Outline each blood parasite and name the species.
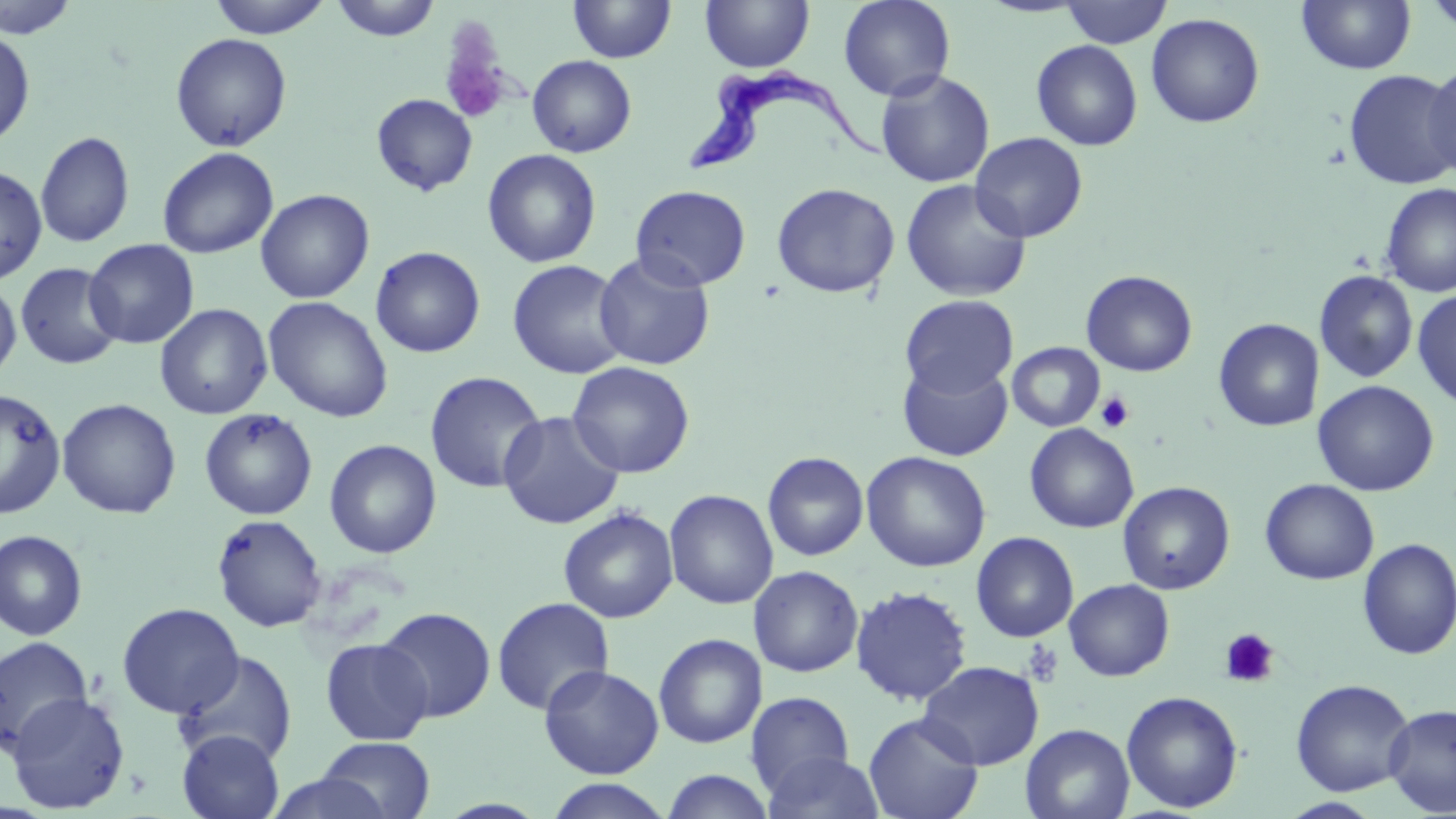

Approximate bounding boxes as (x1,y1)-(x2,y2) corner pairs in pixels.
Trypanosoma brucei: (683,72)-(892,177).
No Plasmodium falciparum, Plasmodium ovale, Plasmodium malariae, Plasmodium vivax, or Babesia divergens observed.

Platelet locations: (438,26)-(513,125), (1095,391)-(1134,433), (1219,628)-(1279,687), (1022,640)-(1064,688). Uninfected red blood cell locations: (0,0)-(82,39), (206,0)-(333,38), (329,0)-(442,41), (568,0)-(676,63), (699,0)-(815,73), (838,0)-(956,101), (1059,0)-(1172,48), (1297,0)-(1416,75), (1421,0)-(1456,37), (1146,13)-(1265,128), (0,26)-(36,149), (170,33)-(292,152), (1031,40)-(1143,151), (527,55)-(636,157), (1423,61)-(1456,180), (875,70)-(995,187), (1344,70)-(1456,190), (371,93)-(478,196), (35,130)-(135,248), (970,131)-(1088,242), (157,146)-(278,259), (482,149)-(601,268), (0,165)-(48,285), (900,179)-(1032,302), (771,182)-(900,299), (1379,182)-(1456,298), (630,185)-(751,291), (256,189)-(374,304), (84,239)-(199,349), (370,246)-(486,358), (593,251)-(716,371), (507,259)-(631,379), (15,262)-(124,369), (1081,270)-(1198,377), (1314,270)-(1418,383), (0,279)-(22,383), (1412,289)-(1456,409), (900,294)-(1018,397), (263,296)-(394,422), (154,303)-(273,420), (1214,318)-(1323,432), (1007,342)-(1105,432), (897,360)-(1013,461), (567,361)-(695,478), (424,371)-(546,494), (1313,380)-(1438,496), (0,388)-(67,520), (57,398)-(182,519), (199,408)-(318,520), (499,410)-(625,530), (1024,423)-(1139,533), (324,438)-(442,559), (762,451)-(869,561), (861,451)-(991,572), (1260,478)-(1379,585), (1118,481)-(1235,595), (664,488)-(779,609), (558,506)-(679,623), (211,513)-(328,633), (0,530)-(88,641), (970,531)-(1079,642), (1356,538)-(1456,660), (748,565)-(864,678), (1064,579)-(1175,681), (850,585)-(973,707), (492,597)-(615,716), (117,603)-(244,719), (376,607)-(495,722), (653,633)-(767,749), (0,636)-(94,754), (320,638)-(433,746), (174,651)-(298,767), (917,660)-(1045,770), (539,664)-(664,779), (1290,678)-(1415,796), (1121,690)-(1244,813), (4,691)-(130,813), (745,691)-(855,797), (1384,704)-(1456,816), (863,713)-(983,819), (1020,723)-(1135,819), (177,729)-(285,819), (315,736)-(437,819), (763,750)-(885,819), (660,769)-(776,818), (263,772)-(396,819), (543,778)-(675,818), (1279,798)-(1386,818). Slide-level diagnosis: Trypanosoma brucei. Thin blood smear. Optical microscopy. Image is 1456×819 pixels. May-Grünwald-Giemsa stain. Captured at 1000x magnification. One field of a larger specimen.